Identify the preparation type.
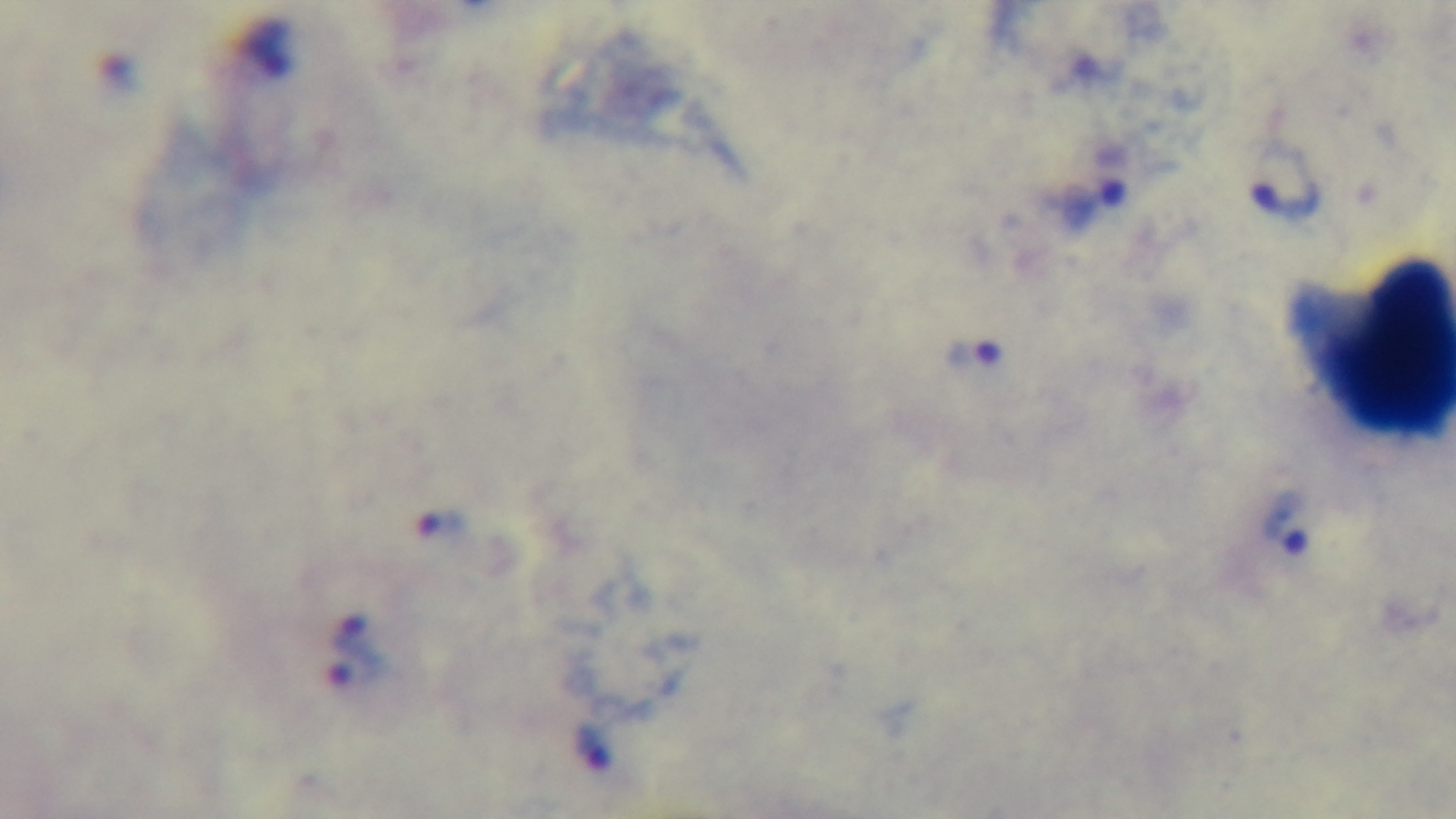

A thick smear.

{
  "capture": "mounted 4K digital camera",
  "field_of_view": "single",
  "stain": "Giemsa",
  "malaria_status": "positive",
  "objective": "100x oil immersion",
  "modality": "light microscopy"
}